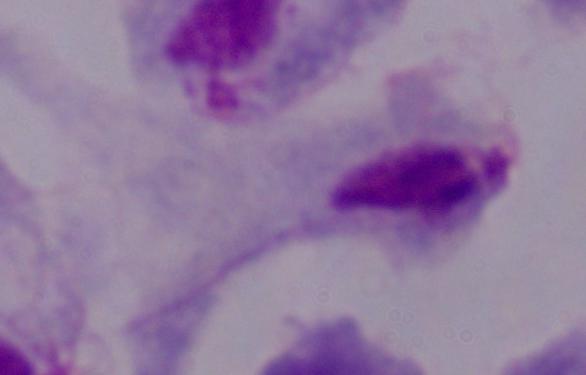

modality = micrograph
identification = trichomonad
magnification = 1000x